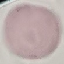

Summary:
  - Malaria status: uninfected
  - Capture: smartphone camera at the microscope eyepiece
  - Preparation: thin blood film
  - Stain: Giemsa
  - Image type: cell patch, automatically extracted from a larger field of view and resized to 64 × 64 pixels